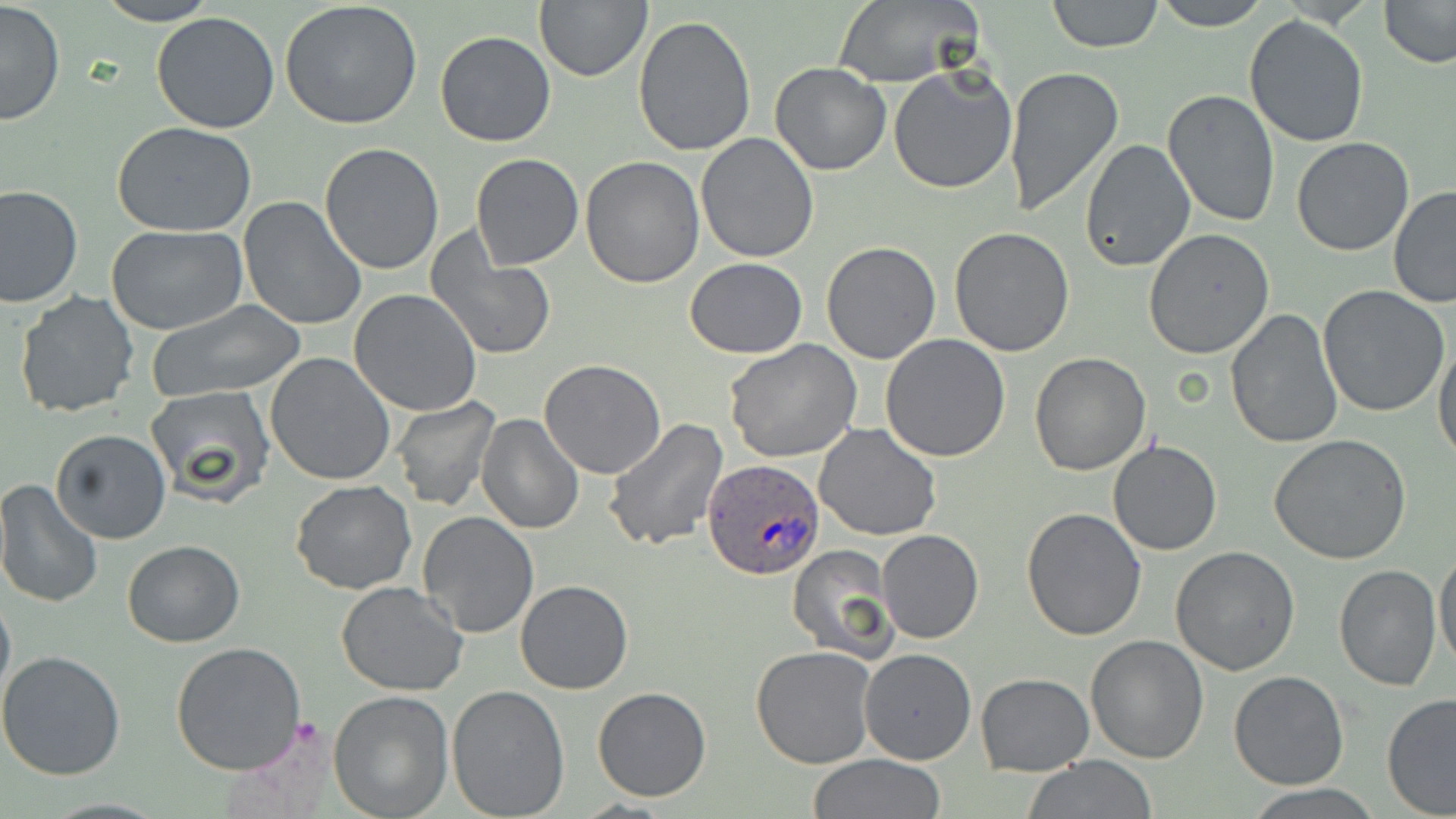
slide-level diagnosis = Plasmodium ovale
preparation = thin blood smear
magnification = 1000x
field of view = single
stain = May-Grünwald-Giemsa
image size = 1456×819 pixels
Plasmodium ovale-infected red blood cell locations = approximate bounding boxes as [x1, y1, x2, y2] in pixels: [704, 457, 828, 581]
uninfected red blood cell locations = approximate bounding boxes as [x1, y1, x2, y2] in pixels: [1046, 0, 1164, 53], [1149, 0, 1274, 30], [1376, 0, 1456, 68], [0, 1, 66, 126], [93, 1, 220, 26], [534, 1, 651, 82], [281, 2, 424, 132], [832, 2, 982, 87], [150, 11, 281, 134], [1242, 13, 1369, 148], [632, 14, 758, 158], [434, 30, 558, 147], [769, 62, 892, 176], [888, 65, 1018, 194], [1003, 65, 1123, 217], [1162, 89, 1280, 227], [113, 122, 259, 237], [696, 133, 821, 263], [1078, 138, 1196, 272], [1292, 138, 1414, 256], [319, 142, 445, 276], [470, 152, 584, 271], [580, 155, 706, 289], [0, 184, 83, 309], [1388, 186, 1456, 308], [238, 197, 367, 333], [105, 224, 249, 334], [949, 227, 1077, 357], [1142, 228, 1275, 358], [425, 234, 556, 361], [822, 242, 941, 364], [685, 258, 808, 357], [1317, 285, 1451, 418], [349, 289, 482, 416], [16, 291, 140, 417], [146, 299, 308, 403], [1225, 310, 1341, 449], [880, 334, 1011, 462], [1432, 337, 1456, 465], [723, 341, 862, 463], [265, 352, 396, 485], [1028, 352, 1151, 476], [539, 359, 668, 479], [144, 386, 275, 507], [389, 396, 500, 511], [477, 412, 585, 533], [604, 418, 729, 553], [814, 423, 942, 542], [51, 428, 171, 544], [1268, 433, 1411, 564], [1108, 438, 1222, 556], [0, 480, 103, 609], [291, 480, 417, 594], [1021, 508, 1148, 643], [418, 512, 538, 640], [878, 530, 985, 644], [122, 538, 245, 649], [1434, 543, 1456, 673], [786, 544, 900, 663], [1169, 546, 1299, 676], [1333, 563, 1442, 691], [515, 578, 634, 695], [336, 582, 468, 696], [0, 586, 15, 709], [1085, 635, 1209, 763], [172, 641, 307, 775], [750, 645, 876, 768], [859, 648, 977, 765], [0, 649, 127, 779], [976, 671, 1094, 775], [1229, 671, 1348, 790], [445, 682, 569, 818], [591, 686, 712, 802], [328, 689, 455, 818], [1381, 692, 1456, 817], [805, 754, 949, 817], [1019, 756, 1160, 818], [1239, 783, 1388, 817]
modality = light microscopy